Assess this cell for malaria.
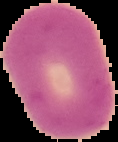

It is uninfected.

From a thin blood film. Image is 118×142 pixels. The area outside the segmented cell region is set to black.